Comment on the morphology of the red blood cells.
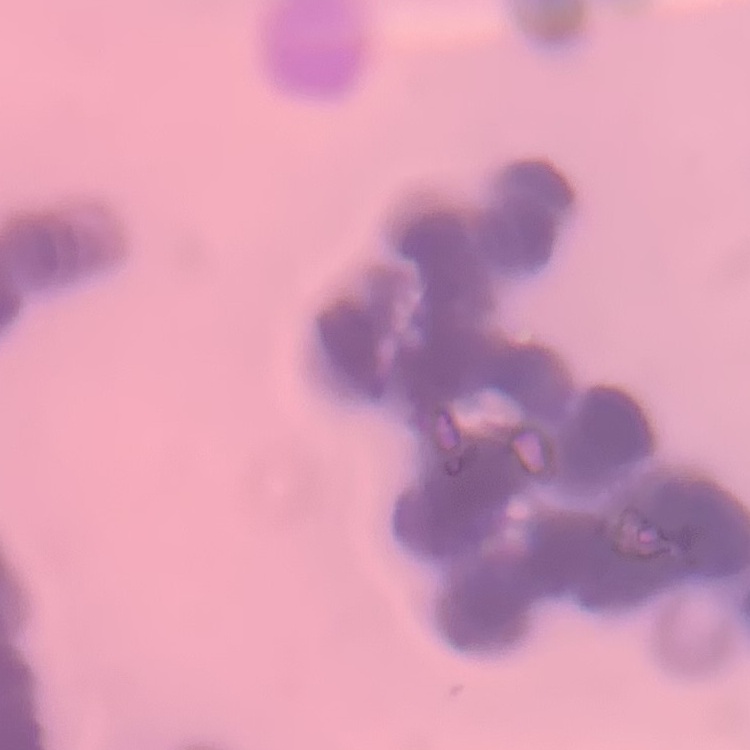

Rouleaux formation.

{
  "stain": "Field's or Giemsa",
  "image_type": "one tile cut from a larger photomicrograph",
  "preparation": "thin blood smear"
}